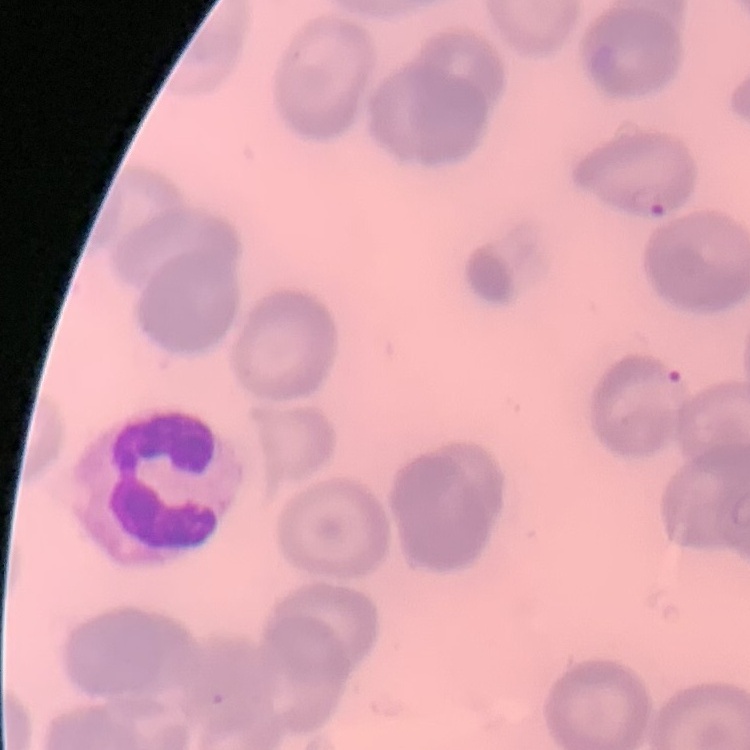
red blood cell morphology = no rouleaux formation
stain = Field's or Giemsa
image type = one tile cut from a larger photomicrograph
preparation = thin blood film